Assess this cell for malaria.
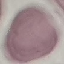

It is uninfected.

preparation = thin blood film
image type = cell patch, automatically extracted from a larger field of view and resized to 64 × 64 pixels
capture = smartphone through the microscope eyepiece
stain = Giemsa